Assess this cell for malaria.
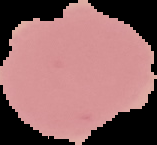

It is uninfected.

From a thin blood smear. The area outside the segmented cell region is set to black. Image is 157×145 pixels.